Identify the blood parasite species.
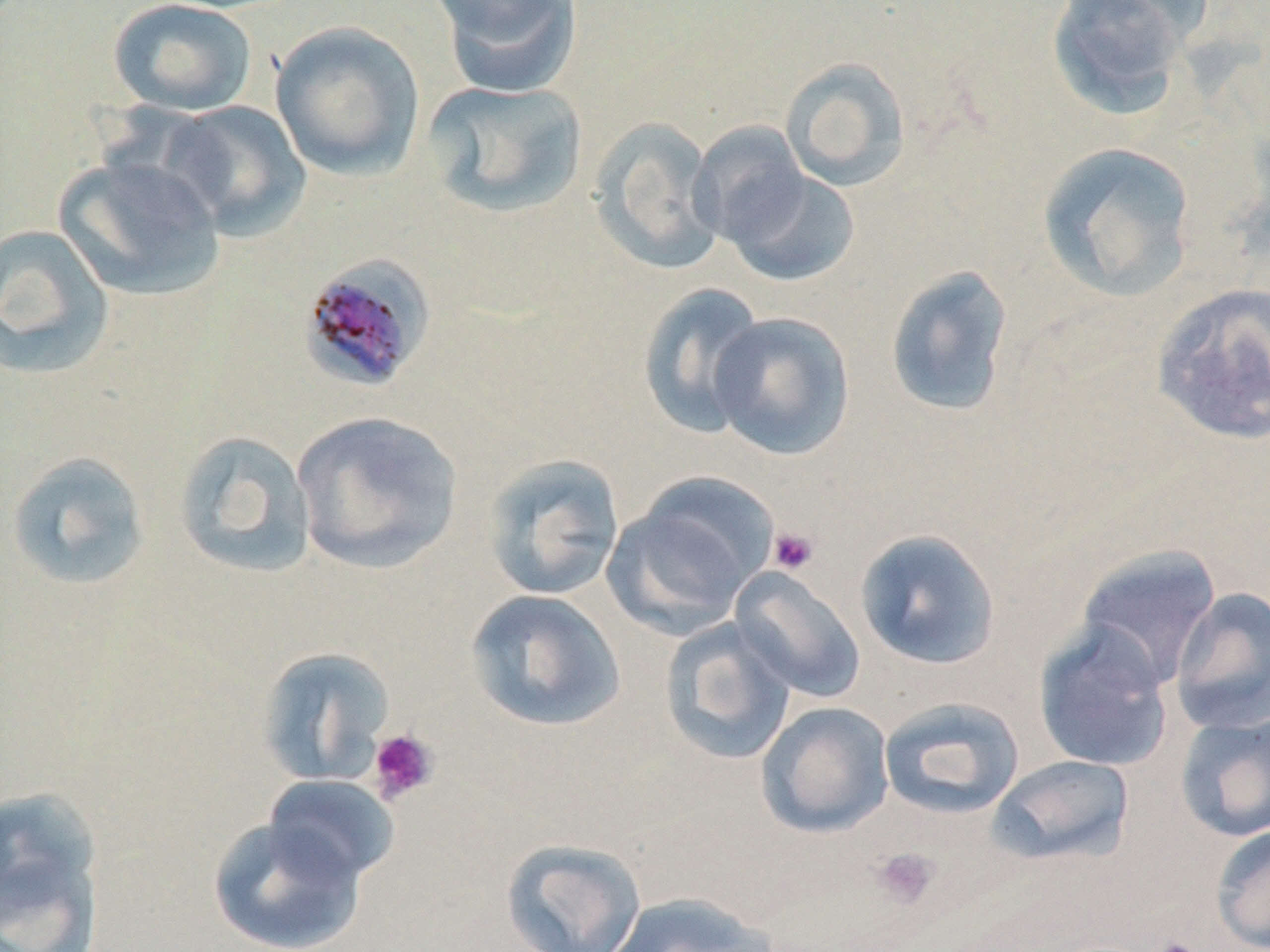
Plasmodium malariae.

Approximate bounding boxes as named x1/y1/x2/y2 corners in pixels. Platelet locations: (x1=768, y1=526, x2=820, y2=575), (x1=366, y1=727, x2=440, y2=805), (x1=871, y1=847, x2=939, y2=910), (x1=1148, y1=936, x2=1204, y2=952). Uninfected red blood cell locations: (x1=108, y1=0, x2=257, y2=117), (x1=433, y1=0, x2=582, y2=97), (x1=1045, y1=0, x2=1201, y2=118), (x1=270, y1=20, x2=426, y2=182), (x1=779, y1=57, x2=913, y2=192), (x1=422, y1=79, x2=589, y2=219), (x1=159, y1=101, x2=312, y2=240), (x1=588, y1=116, x2=726, y2=275), (x1=689, y1=121, x2=810, y2=248), (x1=1035, y1=140, x2=1198, y2=303), (x1=54, y1=153, x2=226, y2=301), (x1=721, y1=165, x2=861, y2=287), (x1=0, y1=224, x2=115, y2=380), (x1=884, y1=264, x2=1015, y2=418), (x1=1150, y1=281, x2=1270, y2=446), (x1=636, y1=282, x2=768, y2=437), (x1=708, y1=310, x2=856, y2=461), (x1=291, y1=409, x2=464, y2=574), (x1=173, y1=429, x2=318, y2=579), (x1=5, y1=451, x2=151, y2=591), (x1=480, y1=453, x2=626, y2=601), (x1=605, y1=476, x2=776, y2=634), (x1=854, y1=528, x2=1003, y2=670), (x1=1074, y1=544, x2=1223, y2=690), (x1=730, y1=567, x2=866, y2=703), (x1=1169, y1=586, x2=1270, y2=734), (x1=463, y1=588, x2=627, y2=733), (x1=659, y1=618, x2=797, y2=765), (x1=1033, y1=621, x2=1176, y2=773), (x1=255, y1=645, x2=396, y2=786), (x1=878, y1=696, x2=1025, y2=819), (x1=755, y1=701, x2=895, y2=838), (x1=1175, y1=711, x2=1270, y2=843), (x1=989, y1=754, x2=1135, y2=867), (x1=261, y1=774, x2=399, y2=886), (x1=0, y1=787, x2=106, y2=948), (x1=207, y1=814, x2=368, y2=952), (x1=1210, y1=824, x2=1270, y2=951), (x1=501, y1=837, x2=647, y2=952), (x1=599, y1=891, x2=780, y2=952). Plasmodium malariae-infected red blood cell locations: (x1=298, y1=252, x2=437, y2=396). Captured at 1000x magnification. Thin blood film. Optical microscopy. May-Grünwald-Giemsa stain. Single field of view. Image is 1270×952 pixels.